Locate every leukocyte (white blood cell).
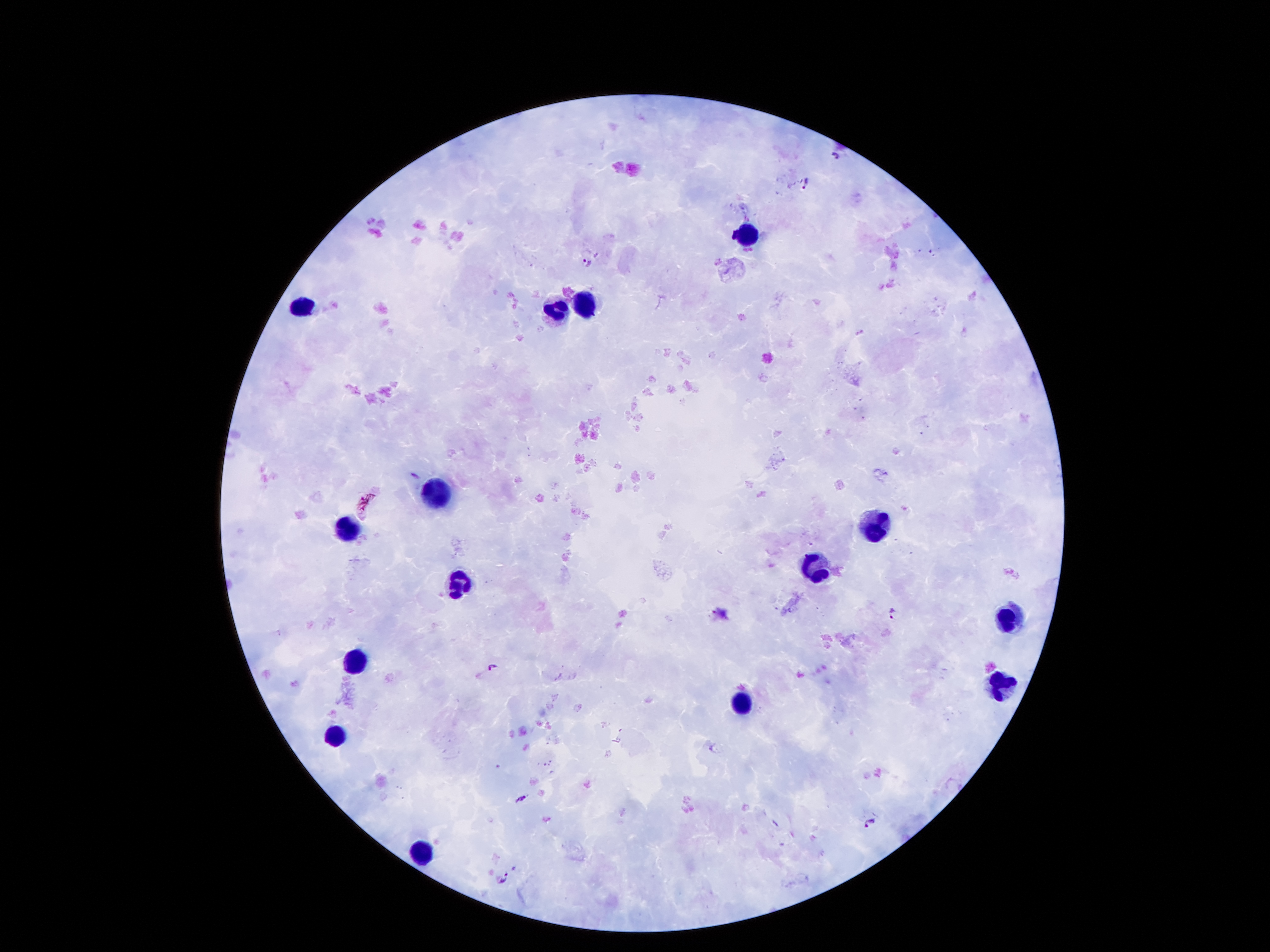
Approximate centers as [x, y] in pixels.
Leukocytes: [749, 236], [303, 305], [589, 305], [556, 315], [438, 492], [875, 523], [344, 529], [814, 563], [457, 582], [1006, 619], [356, 659], [998, 681], [744, 700], [334, 734], [426, 854].

Plasmodium parasite locations: [835, 156], [806, 183], [587, 262], [416, 476], [365, 502], [892, 613], [492, 667], [520, 798], [869, 822], [504, 878]. Smartphone photograph taken through the microscope eyepiece. Image is 1270×952 pixels. Thick peripheral-blood smear. Giemsa-stained preparation. 100x magnification. Single field of view. Patient malaria status: infected with Plasmodium falciparum.